Assess this cell for malaria.
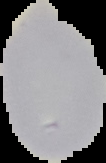

It is uninfected.

From a thin blood smear. The area outside the segmented cell region is set to black. Image is 106×163 pixels.